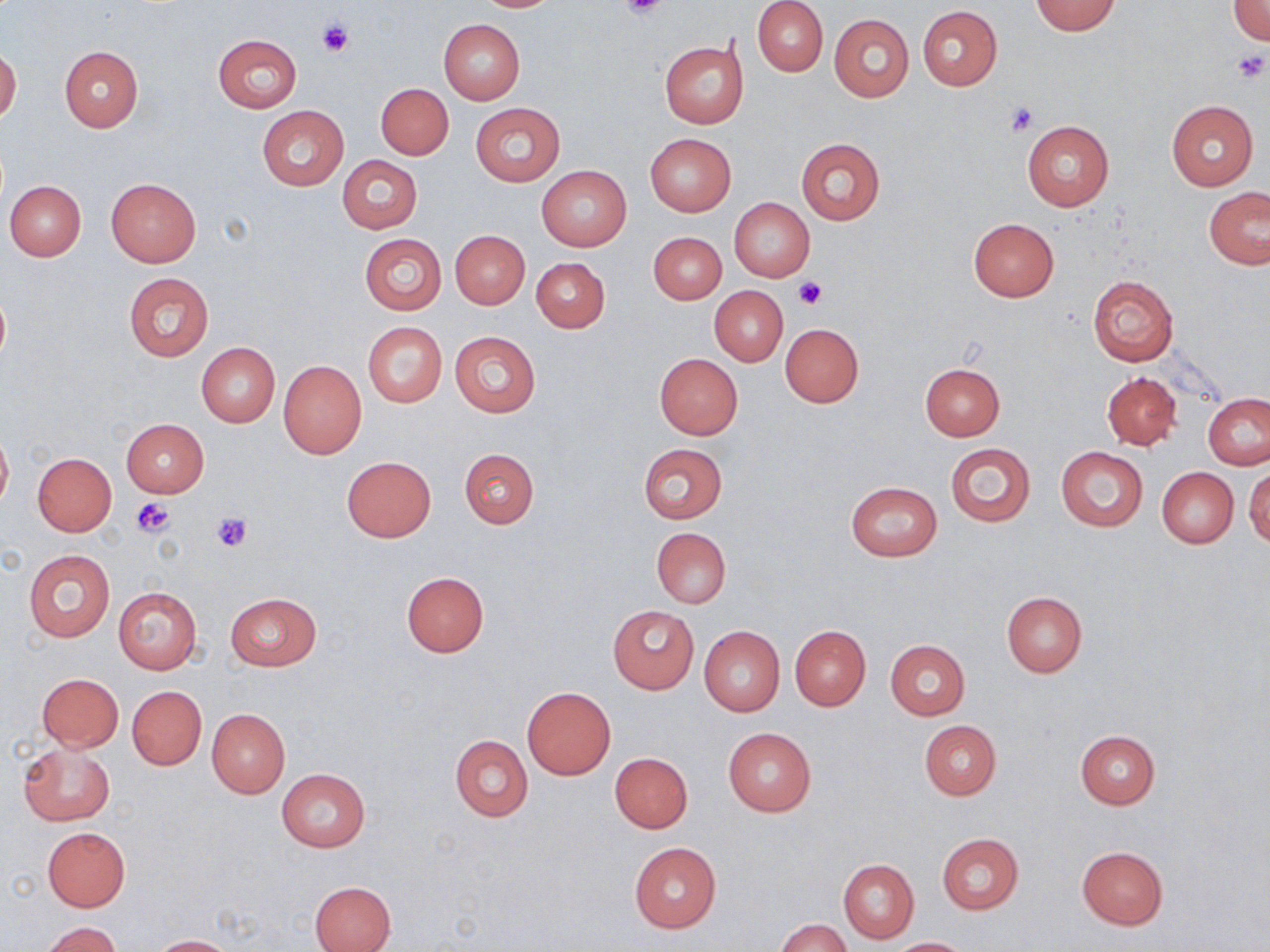

Approximate bounding boxes as (x1, y1, x2, y2) in pixels. Platelet locations: (620, 0, 671, 20), (316, 21, 352, 58), (1230, 49, 1270, 85), (1004, 103, 1038, 136), (792, 278, 826, 308), (133, 497, 177, 538), (209, 510, 252, 553). Uninfected red blood cell locations: (473, 0, 564, 12), (753, 1, 827, 76), (1030, 1, 1121, 35), (1229, 1, 1270, 44), (917, 5, 1001, 91), (828, 13, 914, 103), (439, 19, 524, 104), (212, 33, 303, 113), (659, 40, 748, 129), (59, 46, 143, 132), (0, 48, 21, 124), (377, 83, 453, 159), (1166, 100, 1258, 191), (470, 103, 565, 187), (257, 106, 349, 191), (1021, 119, 1114, 212), (644, 134, 737, 217), (795, 138, 886, 225), (337, 156, 423, 234), (536, 166, 631, 252), (106, 177, 202, 267), (5, 180, 86, 260), (1204, 186, 1270, 269), (729, 198, 815, 282), (968, 218, 1059, 302), (450, 229, 530, 309), (649, 232, 726, 304), (359, 234, 446, 315), (531, 258, 610, 332), (124, 273, 213, 360), (1087, 275, 1178, 367), (0, 285, 10, 370), (709, 286, 788, 366), (363, 322, 447, 408), (780, 323, 863, 407), (449, 331, 541, 418), (196, 343, 280, 426), (655, 354, 743, 438), (279, 360, 366, 459), (919, 362, 1005, 441), (1102, 371, 1182, 450), (1203, 393, 1270, 469), (121, 418, 208, 498), (0, 425, 12, 513), (944, 442, 1036, 528), (637, 443, 728, 525), (1056, 447, 1148, 531), (459, 448, 538, 529), (32, 453, 117, 536), (341, 455, 436, 542), (1245, 465, 1270, 547), (1157, 467, 1238, 548), (845, 480, 942, 562), (651, 528, 731, 608), (22, 549, 115, 642), (400, 571, 490, 657), (113, 587, 202, 674), (1001, 591, 1087, 677), (225, 593, 322, 671), (608, 605, 698, 693), (699, 625, 785, 715), (789, 625, 870, 711), (885, 640, 969, 720), (37, 673, 123, 750), (127, 686, 206, 770), (521, 686, 616, 780), (207, 709, 289, 797), (919, 720, 1001, 800), (723, 727, 816, 816), (1074, 729, 1160, 809), (450, 734, 533, 821), (19, 741, 115, 826), (609, 752, 693, 832), (275, 769, 370, 852), (42, 827, 130, 911), (937, 833, 1025, 915), (630, 843, 721, 932), (1077, 846, 1168, 929), (838, 858, 919, 943), (310, 880, 395, 951), (778, 919, 851, 952), (42, 922, 120, 952), (150, 935, 238, 952), (887, 937, 973, 951). Slide-level diagnosis: no evidence of blood parasites. One field of a larger specimen. Thin blood film. Light microscopy. 1000x magnification. Image is 1270×952 pixels. May-Grünwald-Giemsa stain.